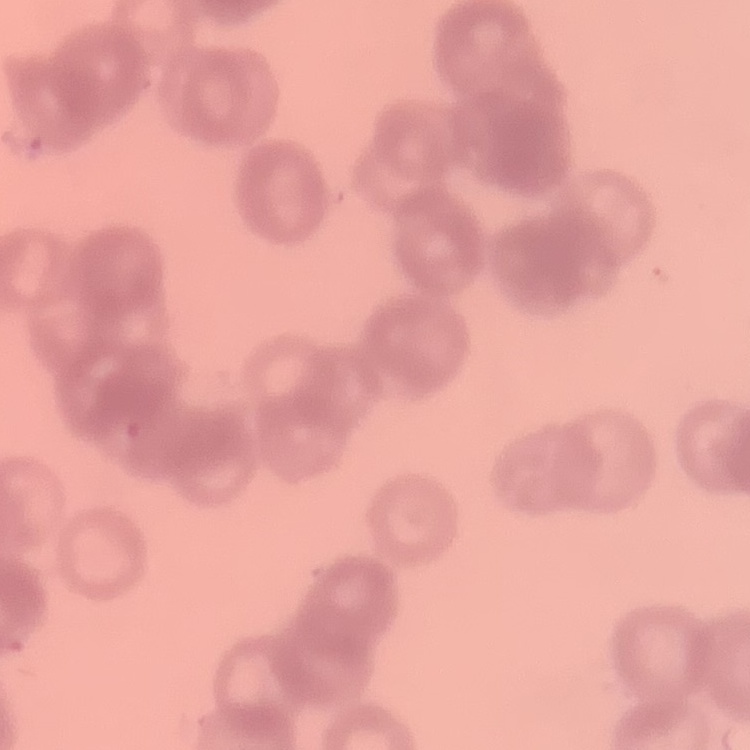

red blood cell morphology = rouleaux formation
preparation = thin blood film
stain = Field's or Giemsa
image type = square crop of a larger photomicrograph